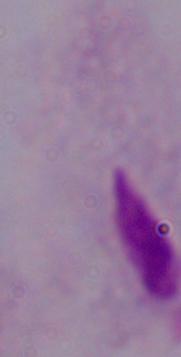
Micrograph. 1000x magnification. A trichomonad is shown.